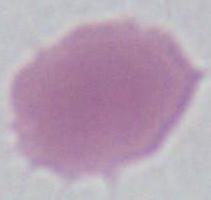

Photomicrograph. 1000x magnification. An erythrocyte is shown.